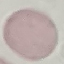
Malaria status: uninfected. Giemsa stain. Cell patch, automatically extracted from a larger field of view and resized to 64 × 64 pixels. Acquired by smartphone through the microscope eyepiece. Thin blood film.